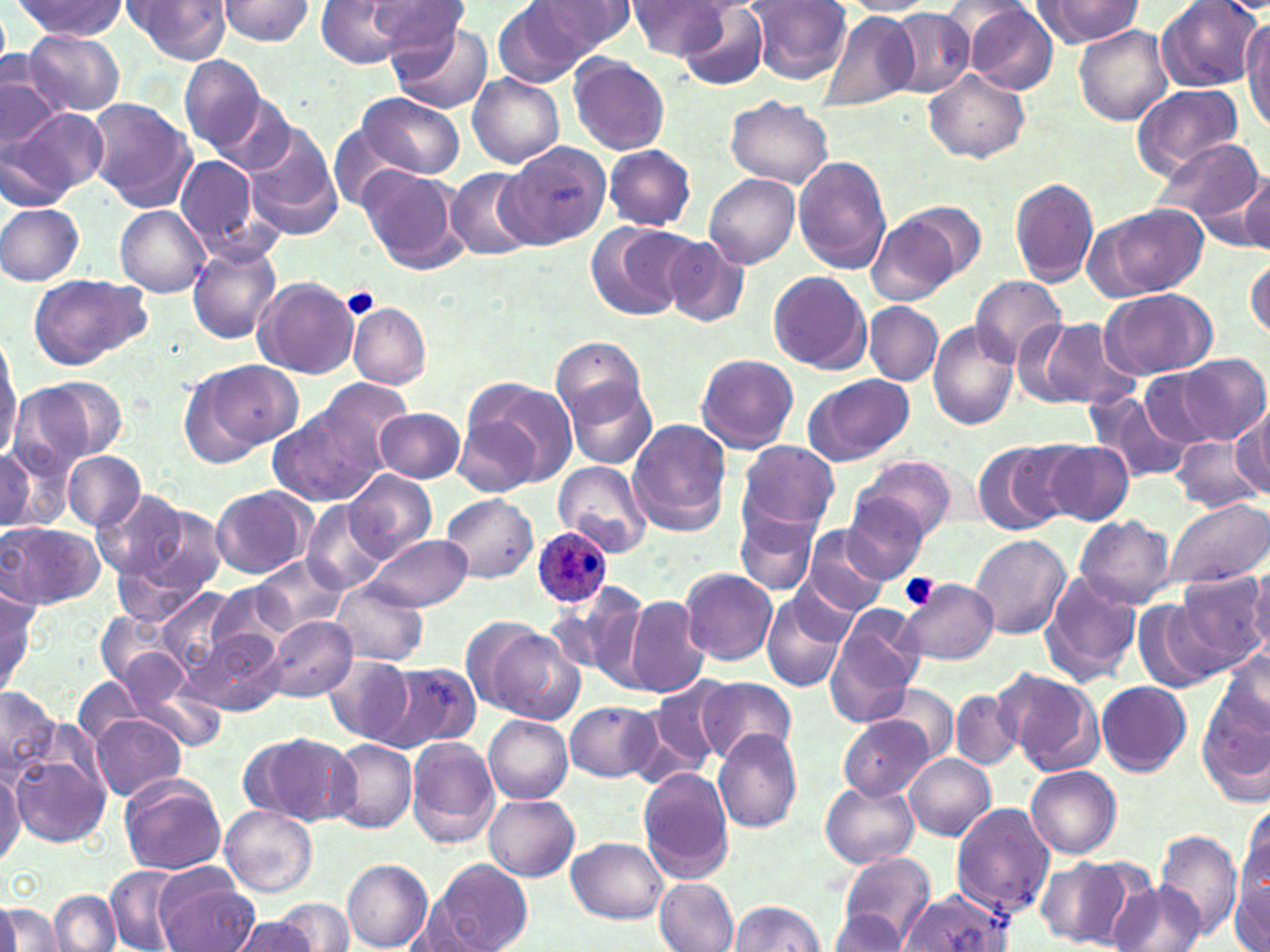
Approximate bounding boxes as (x1, y1, x2, y2) in pixels. Plasmodium ovale-infected red blood cell locations: (530, 526, 614, 608). Platelet locations: (342, 289, 380, 321), (900, 573, 939, 609). Uninfected red blood cell locations: (123, 0, 232, 65), (215, 0, 316, 46), (315, 0, 412, 68), (367, 0, 468, 58), (534, 0, 639, 54), (1033, 0, 1143, 47), (1154, 0, 1262, 92), (493, 1, 602, 84), (625, 1, 732, 58), (747, 1, 853, 83), (832, 1, 938, 15), (11, 2, 129, 41), (964, 2, 1058, 95), (678, 3, 771, 92), (889, 8, 976, 97), (820, 13, 920, 116), (1242, 19, 1270, 131), (388, 22, 494, 114), (1074, 24, 1170, 125), (22, 31, 124, 116), (180, 55, 268, 151), (567, 55, 670, 155), (2, 58, 65, 157), (924, 67, 1029, 164), (468, 73, 564, 167), (1132, 84, 1244, 178), (203, 88, 298, 176), (359, 93, 465, 179), (725, 94, 833, 189), (86, 98, 194, 209), (7, 106, 107, 200), (329, 125, 412, 210), (245, 130, 342, 235), (1151, 136, 1263, 229), (497, 144, 610, 252), (604, 145, 696, 231), (174, 153, 267, 260), (793, 156, 892, 274), (358, 167, 465, 273), (445, 168, 540, 260), (705, 172, 800, 269), (1237, 173, 1270, 254), (1010, 177, 1100, 287), (896, 201, 987, 281), (0, 202, 86, 286), (1092, 203, 1209, 299), (114, 204, 210, 297), (868, 214, 959, 307), (586, 222, 694, 321), (659, 234, 751, 329), (186, 243, 281, 343), (1245, 258, 1270, 342), (768, 270, 871, 374), (27, 271, 153, 371), (254, 276, 359, 378), (971, 276, 1067, 368), (1101, 288, 1215, 379), (348, 302, 431, 389), (863, 302, 943, 385), (1028, 315, 1140, 410), (928, 320, 1019, 430), (0, 337, 22, 458), (553, 339, 650, 425), (694, 353, 799, 455), (1168, 353, 1269, 447), (196, 359, 303, 456), (1139, 366, 1228, 447), (802, 374, 915, 467), (25, 376, 124, 464), (462, 376, 577, 488), (308, 377, 415, 472), (564, 378, 658, 471), (1086, 390, 1186, 484), (1233, 406, 1270, 497), (271, 408, 382, 505), (375, 408, 465, 482), (455, 417, 539, 495), (626, 420, 731, 535), (1168, 434, 1261, 512), (0, 438, 63, 536), (973, 439, 1073, 534), (737, 440, 839, 535), (1039, 440, 1134, 526), (0, 444, 35, 529), (62, 450, 144, 532), (854, 454, 957, 545), (554, 462, 654, 553), (344, 470, 436, 563), (209, 487, 314, 579), (90, 488, 190, 580), (441, 494, 538, 583), (1165, 496, 1269, 590), (842, 497, 933, 580), (301, 501, 385, 596), (123, 505, 227, 608), (734, 511, 819, 597), (1075, 514, 1176, 608), (1, 521, 102, 608), (800, 526, 891, 617), (363, 533, 472, 611), (969, 535, 1070, 638), (253, 554, 349, 634), (681, 567, 777, 664), (1248, 567, 1270, 661), (1172, 569, 1268, 674), (1039, 570, 1142, 685), (901, 577, 998, 665), (331, 581, 427, 666), (207, 583, 292, 660), (554, 587, 650, 683), (0, 588, 41, 696), (158, 589, 241, 674), (760, 591, 852, 692), (624, 596, 709, 695), (1133, 598, 1231, 693), (823, 609, 923, 726), (94, 610, 187, 697), (268, 616, 355, 700), (473, 621, 584, 724), (194, 628, 284, 719), (118, 649, 191, 720), (1217, 650, 1270, 731), (324, 657, 415, 745), (383, 664, 481, 751), (122, 668, 227, 751), (996, 668, 1105, 775), (697, 676, 796, 766), (73, 677, 146, 750), (647, 678, 731, 772), (1095, 681, 1191, 775), (871, 683, 959, 763), (0, 687, 59, 779), (951, 688, 1023, 769), (1198, 692, 1269, 803), (566, 700, 660, 782), (89, 715, 186, 800), (484, 715, 574, 803), (839, 717, 931, 800), (712, 730, 803, 833), (244, 733, 352, 826), (406, 736, 499, 847), (326, 738, 419, 833), (12, 742, 112, 848), (905, 753, 996, 841), (0, 760, 25, 870), (1026, 766, 1122, 860), (638, 769, 734, 882), (120, 775, 226, 874), (820, 781, 919, 868), (485, 794, 579, 881), (950, 803, 1055, 918), (220, 804, 318, 898), (1235, 804, 1268, 931), (1154, 830, 1242, 938), (568, 838, 670, 924), (837, 851, 935, 948), (1040, 856, 1141, 942), (342, 857, 432, 951), (435, 859, 533, 952), (1231, 863, 1270, 952), (104, 867, 184, 951), (157, 867, 257, 952), (654, 877, 739, 952), (1108, 877, 1204, 952), (48, 890, 121, 952), (898, 891, 1015, 952), (275, 898, 356, 951), (2, 900, 63, 951), (727, 900, 824, 952), (828, 909, 909, 950), (230, 916, 322, 952). Slide-level diagnosis: Plasmodium ovale. Image is 1270×952 pixels. May-Grünwald-Giemsa stain. Thin blood film. Light microscopy. One field of a larger specimen. Captured at 1000x magnification.